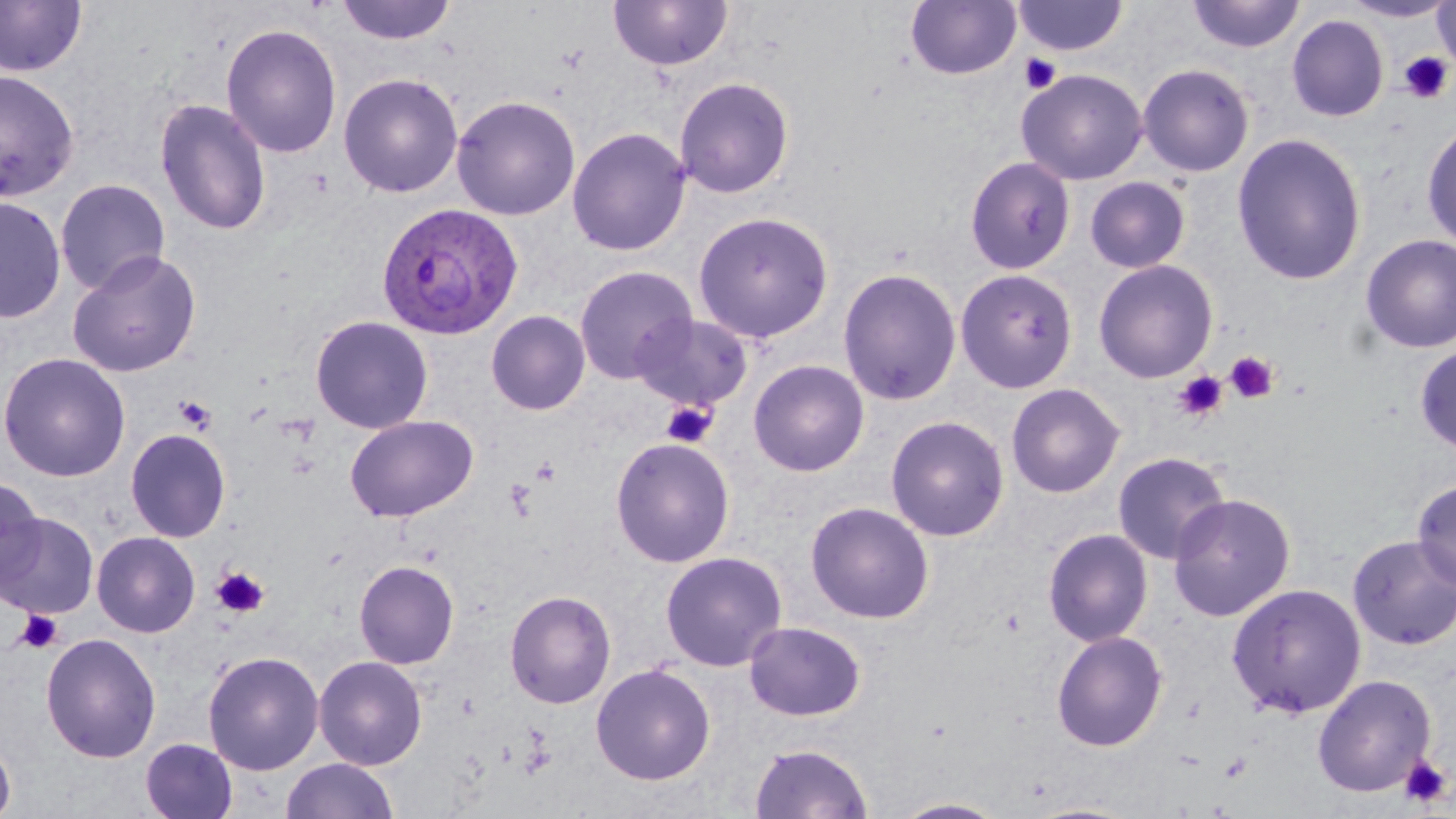

Summary:
  - Coordinate format: approximate bounding boxes as (x1,y1)-(x2,y2) corner pairs in pixels
  - Uninfected red blood cell locations: (336,0)-(456,45), (608,0)-(733,71), (1013,0)-(1128,57), (1186,0)-(1305,53), (0,1)-(87,78), (906,1)-(1022,80), (1340,1)-(1455,23), (1433,1)-(1456,74), (1286,14)-(1389,122), (221,23)-(342,159), (1137,63)-(1255,177), (1016,68)-(1148,185), (0,69)-(79,202), (337,72)-(463,198), (674,76)-(794,199), (450,95)-(581,221), (154,99)-(272,236), (1421,120)-(1456,251), (567,127)-(691,256), (1231,132)-(1368,286), (964,156)-(1076,275), (1085,176)-(1191,273), (55,179)-(170,296), (0,195)-(66,324), (692,211)-(834,344), (1360,233)-(1456,353), (68,250)-(201,377), (1093,259)-(1218,383), (574,264)-(698,384), (837,267)-(962,407), (955,268)-(1078,393), (486,310)-(590,415), (632,313)-(754,411), (310,315)-(433,434), (1413,344)-(1456,456), (0,353)-(131,482), (748,359)-(870,477), (1006,382)-(1125,498), (344,414)-(478,522), (885,415)-(1009,542), (125,428)-(231,542), (610,437)-(736,568), (1112,451)-(1230,564), (0,475)-(43,588), (1411,477)-(1456,592), (1168,493)-(1296,621), (804,500)-(935,624), (0,511)-(98,618), (1042,528)-(1153,647), (92,531)-(200,637), (1347,534)-(1456,651), (660,551)-(787,671), (354,560)-(459,669), (1226,583)-(1366,718), (504,590)-(616,709), (743,620)-(866,721), (1051,630)-(1168,752), (41,632)-(161,763), (202,650)-(325,775), (313,656)-(428,769), (590,662)-(715,785), (1313,674)-(1437,798), (0,736)-(15,819), (140,737)-(238,819), (748,742)-(875,818), (281,757)-(399,818), (890,797)-(1010,818), (1023,800)-(1140,818)
  - Plasmodium ovale-infected red blood cell locations: (376,202)-(524,340)
  - Platelet locations: (1398,51)-(1453,104), (1019,53)-(1061,94), (1225,351)-(1280,404), (1173,370)-(1229,421), (175,395)-(217,434), (661,401)-(718,449), (530,456)-(561,486), (505,478)-(537,518), (211,567)-(269,618), (15,609)-(63,654), (1219,752)-(1253,782), (1399,754)-(1451,807)
  - Slide-level diagnosis: Plasmodium ovale
  - Field of view: single
  - Preparation: thin blood smear
  - Image size: 1456×819 pixels
  - Magnification: 1000x
  - Modality: optical microscopy
  - Stain: May-Grünwald-Giemsa